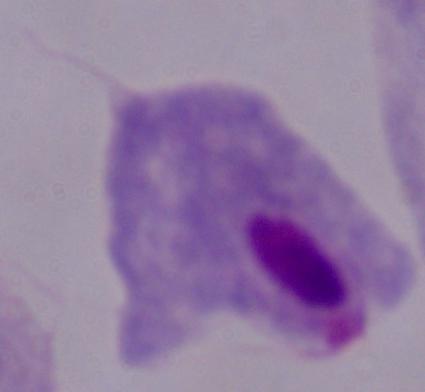
Captured at 1000x magnification. A trichomonad is shown. Photomicrograph.